Assess the morphology of the red blood cells.
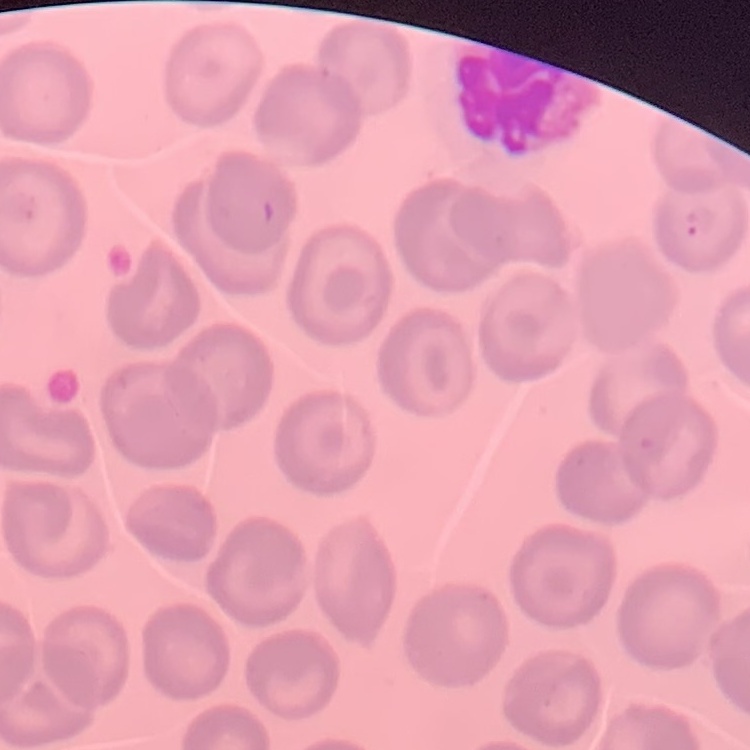

They show no rouleaux formation.

Summary:
  - Stain: Field's or Giemsa
  - Image type: one tile cut from a larger photomicrograph
  - Preparation: thin blood smear